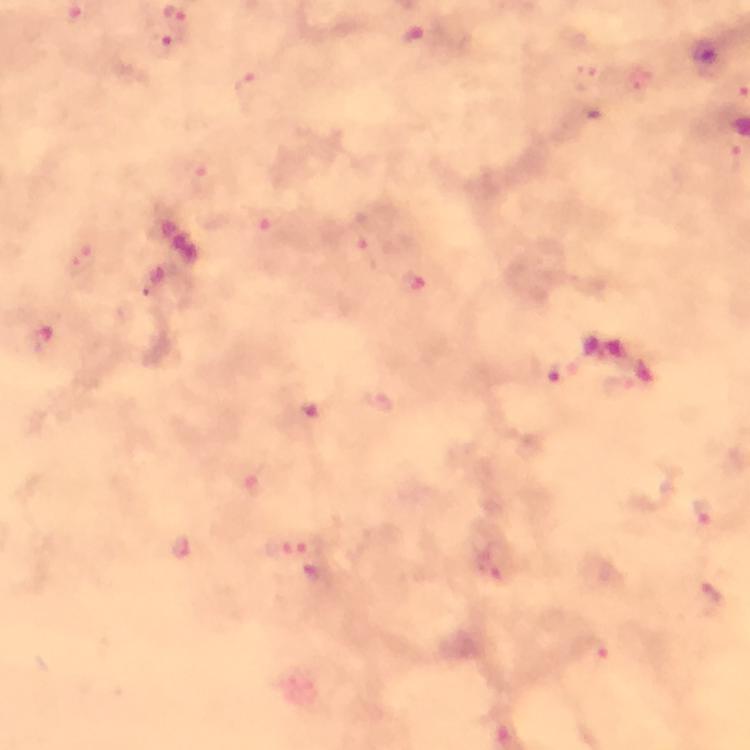 Approximate centers as (x, y) in pixels. Plasmodium parasite locations: (164, 47), (705, 55), (585, 77), (247, 91), (198, 171), (365, 252), (83, 263), (416, 282), (563, 372), (380, 401), (704, 512), (309, 543), (183, 549), (488, 566), (708, 597), (594, 651). Giemsa stain. A crop from one field of view. 100x magnification. Immersion oil was used. Image is 750×750 pixels. Smartphone photograph taken through a microscope. From a malaria diagnostic workup. Thick blood smear.